Classify this cell by malaria status.
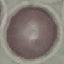

Uninfected.

Giemsa-stained preparation. Thin blood smear. Cell patch, automatically extracted from a larger field of view and resized to 64 × 64 pixels. Acquired by smartphone through the microscope eyepiece.